Locate every Plasmodium parasite.
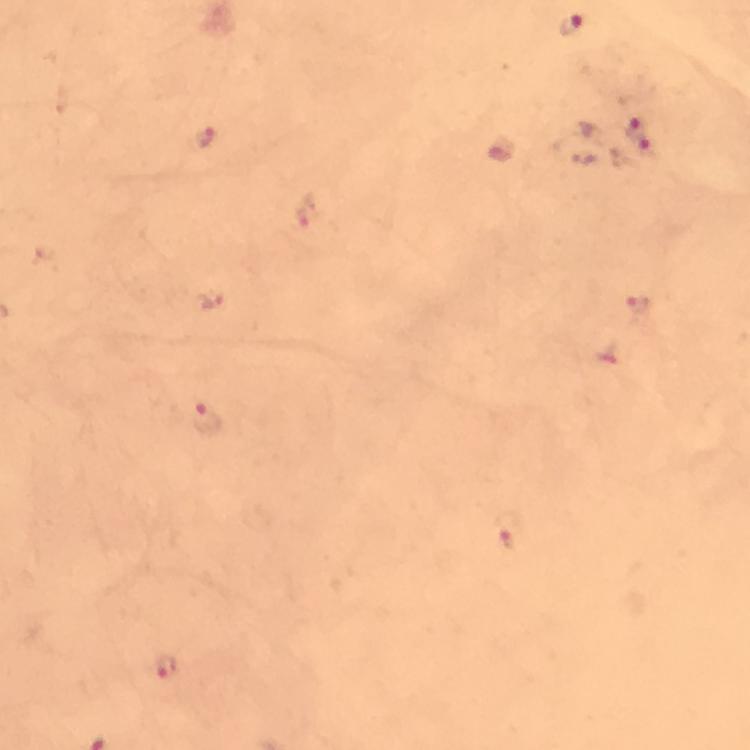

Approximate centers as {x, y} in pixels.
Plasmodium parasites: {571, 24}, {633, 125}, {205, 136}, {648, 150}, {308, 212}, {637, 305}, {208, 420}, {510, 533}, {166, 668}.

image size = 750×750 pixels
preparation = thick blood smear
cropped from = one field of view
magnification = 100x
context = from a malaria diagnostic workup
immersion oil = used
capture = smartphone mounted on the microscope
stain = Giemsa